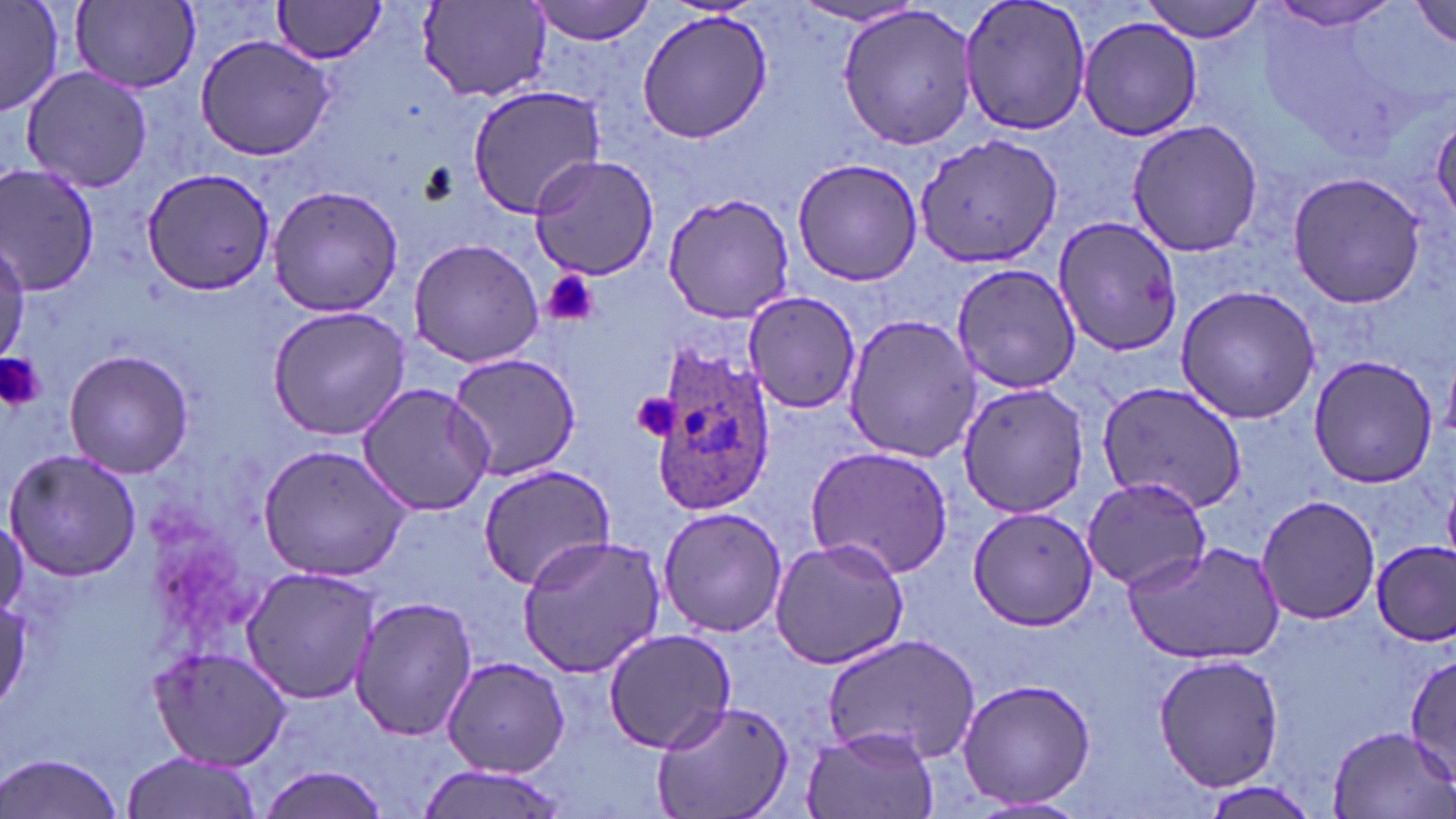
slide_level_diagnosis: Plasmodium ovale
modality: optical microscopy
field_of_view: single
stain: May-Grünwald-Giemsa
image_size: 1456×819 pixels
plasmodium_ovale_infected_red_blood_cell_locations: 'approximate bounding boxes as named x1/y1/x2/y2 corners in pixels: (x1=649, y1=348, x2=777, y2=514)'
preparation: thin blood film
platelet_locations: 'approximate bounding boxes as named x1/y1/x2/y2 corners in pixels: (x1=543, y1=269, x2=599, y2=328), (x1=0, y1=354, x2=45, y2=414), (x1=632, y1=391, x2=681, y2=442)'
magnification: 1000x
uninfected_red_blood_cell_locations: 'approximate bounding boxes as named x1/y1/x2/y2 corners in pixels: (x1=0, y1=0, x2=64, y2=116), (x1=530, y1=0, x2=659, y2=44), (x1=956, y1=0, x2=1095, y2=137), (x1=1140, y1=0, x2=1268, y2=42), (x1=70, y1=1, x2=201, y2=92), (x1=269, y1=1, x2=391, y2=62), (x1=417, y1=1, x2=553, y2=100), (x1=1263, y1=2, x2=1407, y2=32), (x1=1413, y1=2, x2=1456, y2=49), (x1=791, y1=3, x2=927, y2=31), (x1=835, y1=5, x2=979, y2=150), (x1=637, y1=10, x2=771, y2=142), (x1=1077, y1=16, x2=1203, y2=142), (x1=193, y1=32, x2=339, y2=161), (x1=20, y1=65, x2=154, y2=193), (x1=466, y1=85, x2=605, y2=217), (x1=1124, y1=118, x2=1263, y2=256), (x1=912, y1=133, x2=1065, y2=270), (x1=527, y1=154, x2=664, y2=282), (x1=791, y1=157, x2=926, y2=287), (x1=0, y1=165, x2=99, y2=297), (x1=142, y1=168, x2=275, y2=296), (x1=1287, y1=171, x2=1429, y2=309), (x1=268, y1=185, x2=404, y2=318), (x1=662, y1=193, x2=798, y2=323), (x1=1051, y1=213, x2=1183, y2=359), (x1=408, y1=238, x2=545, y2=369), (x1=0, y1=239, x2=28, y2=363), (x1=949, y1=263, x2=1080, y2=394), (x1=1173, y1=285, x2=1320, y2=425), (x1=742, y1=289, x2=863, y2=412), (x1=265, y1=304, x2=410, y2=441), (x1=840, y1=311, x2=982, y2=463), (x1=64, y1=350, x2=193, y2=479), (x1=445, y1=351, x2=583, y2=482), (x1=1307, y1=353, x2=1438, y2=489), (x1=1097, y1=379, x2=1247, y2=511), (x1=356, y1=382, x2=494, y2=517), (x1=955, y1=383, x2=1092, y2=519), (x1=258, y1=444, x2=413, y2=581), (x1=805, y1=446, x2=956, y2=577), (x1=5, y1=450, x2=142, y2=581), (x1=475, y1=464, x2=620, y2=593), (x1=1080, y1=473, x2=1215, y2=591), (x1=1255, y1=493, x2=1382, y2=627), (x1=656, y1=504, x2=787, y2=640), (x1=967, y1=505, x2=1099, y2=631), (x1=515, y1=531, x2=668, y2=678), (x1=768, y1=536, x2=910, y2=670), (x1=1121, y1=541, x2=1285, y2=664), (x1=1372, y1=542, x2=1455, y2=646), (x1=239, y1=567, x2=381, y2=704), (x1=347, y1=594, x2=478, y2=743), (x1=0, y1=598, x2=29, y2=711), (x1=603, y1=629, x2=735, y2=753), (x1=817, y1=631, x2=981, y2=766), (x1=148, y1=645, x2=294, y2=771), (x1=1152, y1=651, x2=1284, y2=794), (x1=1404, y1=652, x2=1456, y2=785), (x1=440, y1=655, x2=569, y2=777), (x1=956, y1=676, x2=1097, y2=811), (x1=650, y1=697, x2=794, y2=819), (x1=1324, y1=724, x2=1454, y2=818), (x1=801, y1=725, x2=941, y2=819), (x1=120, y1=751, x2=265, y2=819), (x1=0, y1=752, x2=126, y2=819), (x1=412, y1=764, x2=572, y2=819), (x1=254, y1=766, x2=389, y2=819), (x1=1188, y1=780, x2=1326, y2=819)'